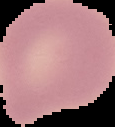

From a thin blood smear. Cell region segmented out of the field of view; the surrounding area is masked to black. Image is 115×127 pixels. Malaria status: uninfected.